Comment on the morphology of the red blood cells.
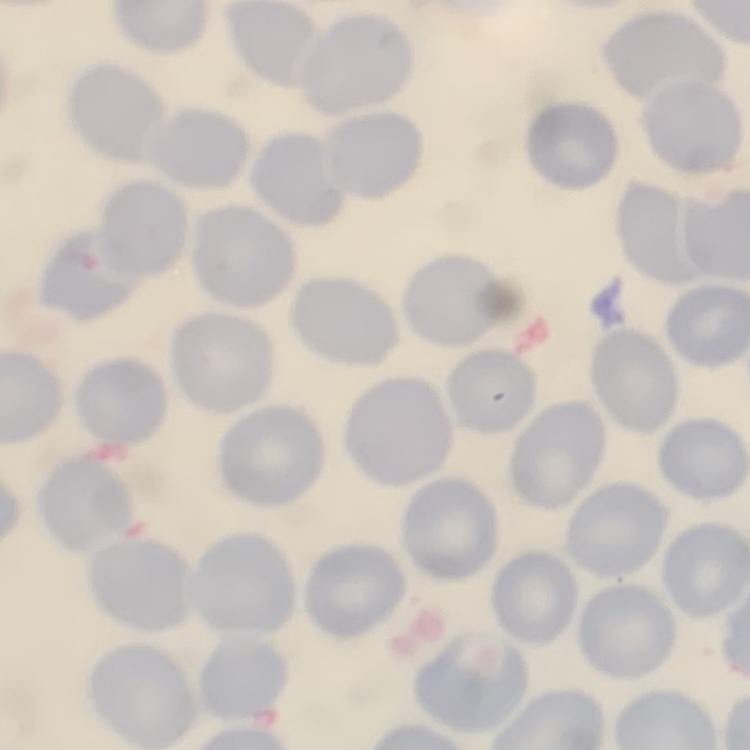

No rouleaux formation.

preparation = thin blood film
stain = Field's or Giemsa
image type = one tile cut from a larger photomicrograph